Report the malaria status of this cell.
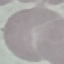

Uninfected.

preparation = thin blood smear
capture = smartphone through the microscope eyepiece
image type = cell patch, automatically extracted from a larger field of view and resized to 64 × 64 pixels
stain = Giemsa